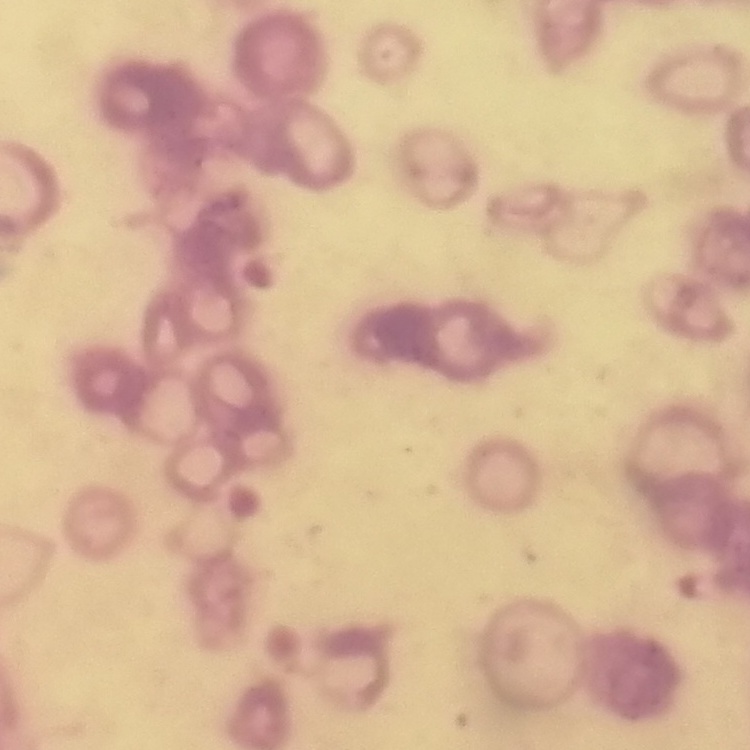

erythrocyte morphology = rouleaux formation
image type = square crop of a larger photomicrograph
preparation = thin blood smear
stain = Field's or Giemsa